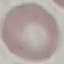
malaria status = uninfected
stain = Giemsa
image type = automatically extracted cell patch, resized to 64 × 64 pixels
preparation = thin blood smear
capture = smartphone camera at the microscope eyepiece